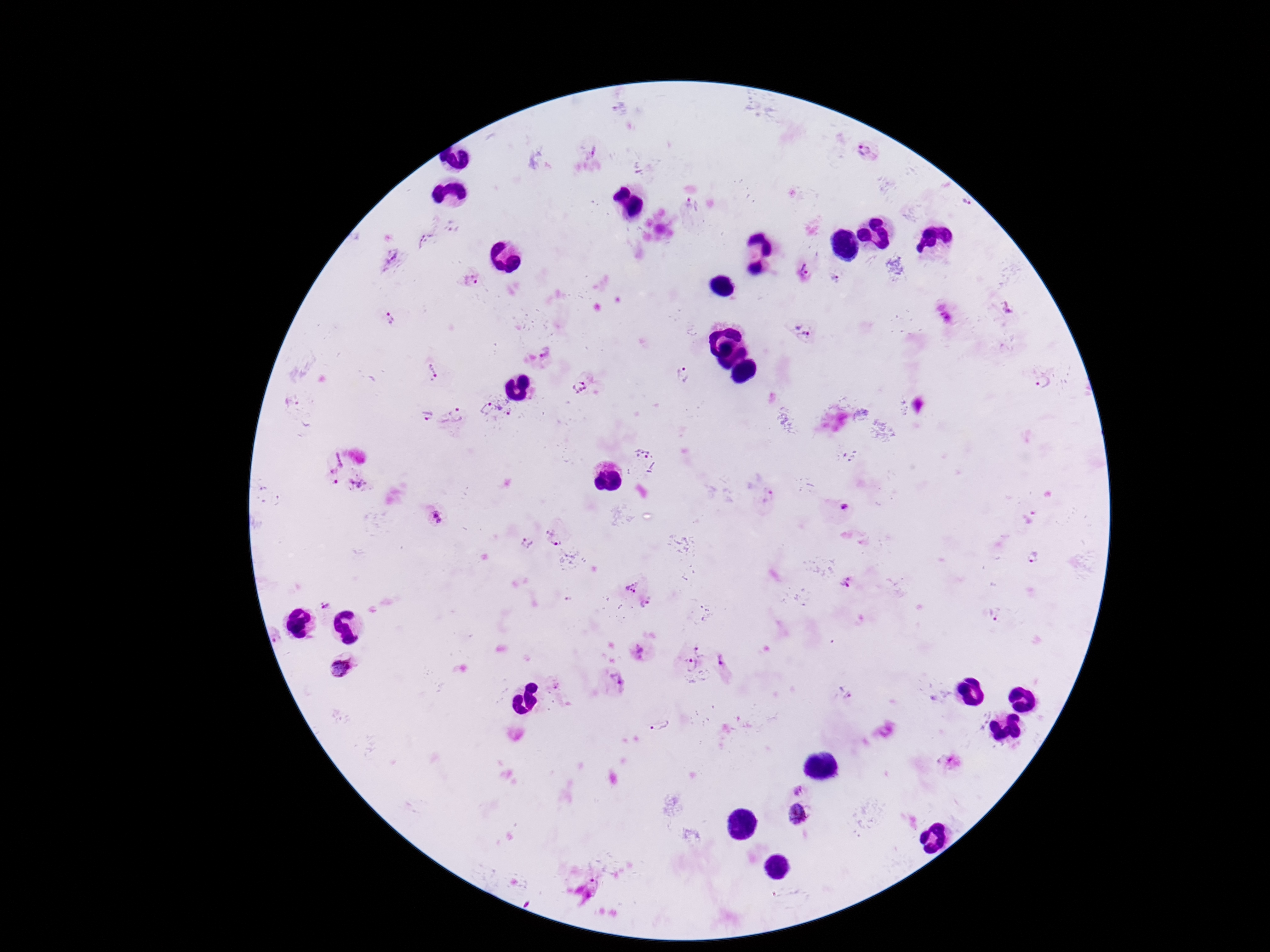
Approximate centers as {x, y} in pixels.
Summary:
  - Plasmodium parasite locations: {868, 150}, {967, 204}, {691, 207}, {425, 240}, {390, 258}, {805, 269}, {836, 277}, {470, 280}, {1008, 313}, {390, 317}, {948, 320}, {801, 328}, {433, 373}, {682, 375}, {1042, 382}, {580, 388}, {291, 405}, {486, 405}, {506, 405}, {456, 415}, {426, 417}, {643, 450}, {331, 461}, {335, 481}, {358, 484}, {766, 496}, {844, 506}, {435, 520}, {555, 537}, {527, 543}, {1036, 558}, {845, 582}, {631, 583}, {324, 603}, {645, 603}, {994, 614}, {275, 636}, {700, 647}, {638, 651}, {723, 658}, {690, 668}, {340, 669}, {618, 680}, {556, 686}, {846, 694}, {939, 698}, {661, 725}, {797, 788}, {798, 813}, {594, 883}
  - Magnification: 100x
  - Stain: Giemsa
  - Capture: smartphone camera through the microscope eyepiece
  - Preparation: thick blood film
  - Image size: 1270×952 pixels
  - Field of view: one from this slide
  - Patient malaria status: positive